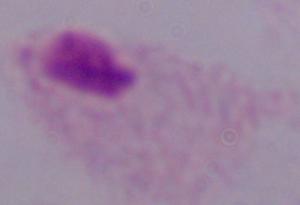
modality = photomicrograph
magnification = 1000x
identification = trichomonad